Locate every blood parasite and identify its species.
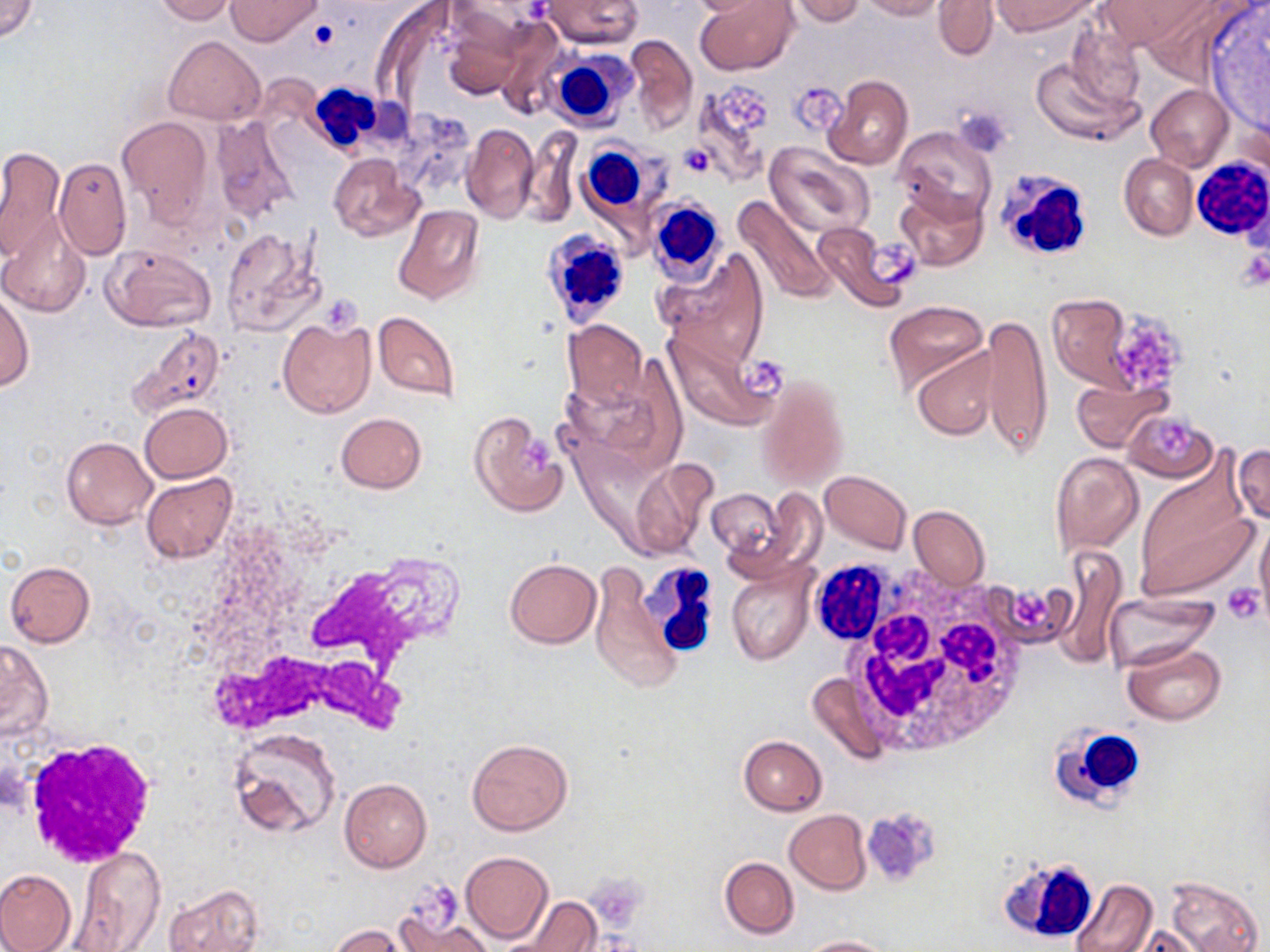

No blood parasites seen.

Approximate bounding boxes as named x1/y1/x2/y2 corners in pixels. Uninfected red blood cell locations: (x1=1, y1=0, x2=38, y2=43), (x1=154, y1=0, x2=236, y2=24), (x1=225, y1=0, x2=321, y2=46), (x1=685, y1=0, x2=780, y2=18), (x1=696, y1=0, x2=799, y2=75), (x1=791, y1=0, x2=865, y2=25), (x1=859, y1=0, x2=942, y2=20), (x1=935, y1=0, x2=997, y2=60), (x1=992, y1=0, x2=1093, y2=34), (x1=1101, y1=0, x2=1207, y2=47), (x1=541, y1=1, x2=642, y2=48), (x1=442, y1=19, x2=524, y2=99), (x1=491, y1=21, x2=568, y2=119), (x1=1066, y1=22, x2=1145, y2=113), (x1=622, y1=33, x2=697, y2=134), (x1=165, y1=36, x2=265, y2=124), (x1=1032, y1=57, x2=1142, y2=148), (x1=824, y1=76, x2=913, y2=170), (x1=691, y1=79, x2=776, y2=185), (x1=1146, y1=84, x2=1233, y2=169), (x1=209, y1=115, x2=300, y2=223), (x1=118, y1=116, x2=212, y2=224), (x1=461, y1=122, x2=539, y2=222), (x1=893, y1=126, x2=999, y2=225), (x1=522, y1=130, x2=580, y2=227), (x1=763, y1=142, x2=875, y2=239), (x1=0, y1=146, x2=64, y2=260), (x1=328, y1=153, x2=423, y2=241), (x1=1121, y1=154, x2=1197, y2=240), (x1=53, y1=158, x2=131, y2=259), (x1=896, y1=187, x2=988, y2=271), (x1=733, y1=192, x2=837, y2=305), (x1=392, y1=206, x2=485, y2=307), (x1=0, y1=211, x2=92, y2=317), (x1=812, y1=219, x2=912, y2=310), (x1=220, y1=226, x2=323, y2=334), (x1=102, y1=244, x2=216, y2=330), (x1=657, y1=250, x2=770, y2=366), (x1=1, y1=290, x2=33, y2=393), (x1=1045, y1=294, x2=1135, y2=390), (x1=883, y1=300, x2=989, y2=396), (x1=373, y1=311, x2=460, y2=402), (x1=980, y1=315, x2=1051, y2=459), (x1=277, y1=318, x2=375, y2=419), (x1=562, y1=320, x2=647, y2=408), (x1=661, y1=322, x2=780, y2=431), (x1=130, y1=327, x2=224, y2=416), (x1=911, y1=346, x2=1001, y2=440), (x1=560, y1=365, x2=686, y2=474), (x1=757, y1=373, x2=848, y2=491), (x1=1072, y1=377, x2=1168, y2=451), (x1=140, y1=402, x2=231, y2=482), (x1=1125, y1=409, x2=1215, y2=482), (x1=467, y1=411, x2=568, y2=516), (x1=336, y1=412, x2=426, y2=493), (x1=61, y1=436, x2=157, y2=529), (x1=1232, y1=443, x2=1269, y2=526), (x1=1050, y1=452, x2=1144, y2=555), (x1=630, y1=456, x2=716, y2=558), (x1=1133, y1=463, x2=1257, y2=603), (x1=820, y1=470, x2=912, y2=554), (x1=140, y1=473, x2=235, y2=564), (x1=707, y1=488, x2=783, y2=560), (x1=909, y1=505, x2=989, y2=590), (x1=1255, y1=519, x2=1270, y2=617), (x1=1053, y1=546, x2=1128, y2=669), (x1=504, y1=559, x2=601, y2=647), (x1=588, y1=560, x2=686, y2=697), (x1=5, y1=561, x2=95, y2=646), (x1=726, y1=561, x2=814, y2=665), (x1=1103, y1=593, x2=1216, y2=672), (x1=0, y1=640, x2=53, y2=742), (x1=1122, y1=640, x2=1226, y2=725), (x1=803, y1=672, x2=888, y2=765), (x1=228, y1=729, x2=341, y2=839), (x1=738, y1=734, x2=826, y2=815), (x1=466, y1=739, x2=572, y2=836), (x1=340, y1=778, x2=432, y2=873), (x1=785, y1=810, x2=872, y2=894), (x1=70, y1=848, x2=165, y2=951), (x1=461, y1=851, x2=552, y2=944), (x1=719, y1=857, x2=798, y2=939), (x1=0, y1=869, x2=78, y2=952), (x1=1164, y1=874, x2=1264, y2=952), (x1=1071, y1=878, x2=1157, y2=952), (x1=165, y1=884, x2=263, y2=952), (x1=391, y1=895, x2=492, y2=952), (x1=512, y1=896, x2=600, y2=952), (x1=329, y1=925, x2=409, y2=952), (x1=1127, y1=925, x2=1210, y2=951), (x1=800, y1=936, x2=894, y2=952). Platelet locations: (x1=718, y1=86, x2=773, y2=136), (x1=797, y1=86, x2=849, y2=131), (x1=954, y1=105, x2=1014, y2=158), (x1=679, y1=144, x2=715, y2=176), (x1=870, y1=238, x2=917, y2=285), (x1=1236, y1=248, x2=1270, y2=291), (x1=325, y1=297, x2=365, y2=339), (x1=1116, y1=314, x2=1184, y2=382), (x1=743, y1=357, x2=787, y2=397), (x1=1158, y1=417, x2=1196, y2=459), (x1=519, y1=438, x2=552, y2=474), (x1=1222, y1=583, x2=1264, y2=625), (x1=1003, y1=584, x2=1066, y2=644), (x1=860, y1=807, x2=942, y2=889), (x1=584, y1=874, x2=648, y2=925), (x1=406, y1=881, x2=462, y2=939). White blood cell locations: (x1=544, y1=47, x2=637, y2=131), (x1=306, y1=83, x2=386, y2=155), (x1=580, y1=144, x2=651, y2=217), (x1=1192, y1=159, x2=1270, y2=241), (x1=1000, y1=170, x2=1091, y2=257), (x1=647, y1=197, x2=727, y2=290), (x1=539, y1=226, x2=631, y2=330), (x1=223, y1=557, x2=448, y2=737), (x1=816, y1=560, x2=906, y2=639), (x1=640, y1=562, x2=721, y2=657), (x1=832, y1=572, x2=1030, y2=756), (x1=1051, y1=725, x2=1150, y2=808), (x1=19, y1=736, x2=159, y2=868), (x1=1000, y1=858, x2=1092, y2=937). Slide-level diagnosis: negative for blood parasites. One field of a larger specimen. Light microscopy. May-Grünwald-Giemsa stain. Captured at 1000x magnification. Image is 1270×952 pixels. Thin blood smear.